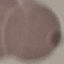

Summary:
  - Malaria status: uninfected
  - Stain: Giemsa
  - Image type: automatically extracted cell patch, resized to 64 × 64 pixels
  - Capture: smartphone through the microscope eyepiece
  - Preparation: thin blood film